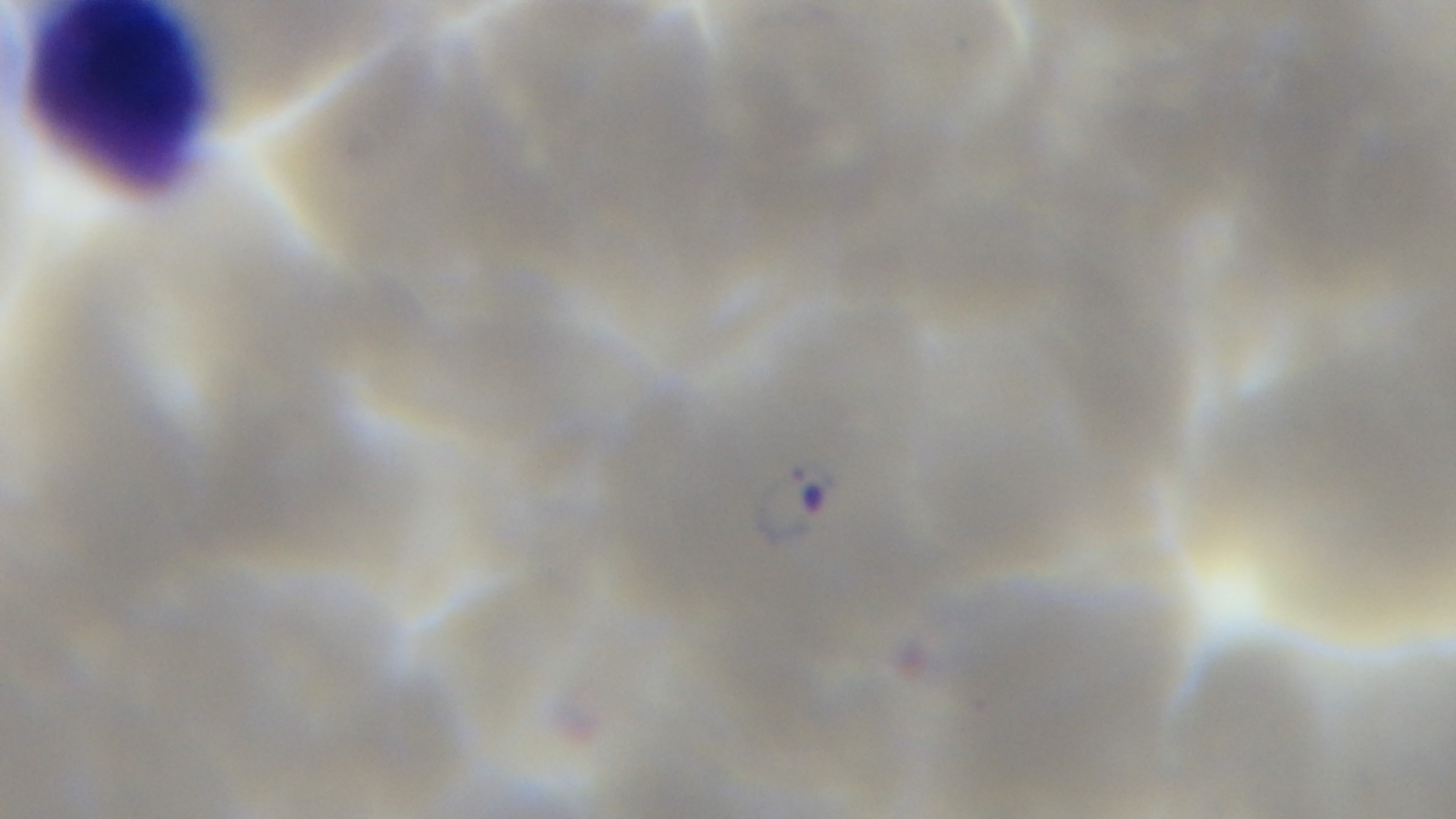
preparation: thin blood film
field_of_view: single
modality: light microscopy
malaria_status: infected
objective: 100x oil immersion
stain: Giemsa
capture: mounted 4K digital camera